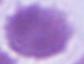
Summary:
  - Magnification: 1000x
  - Modality: micrograph
  - Identification: erythrocyte